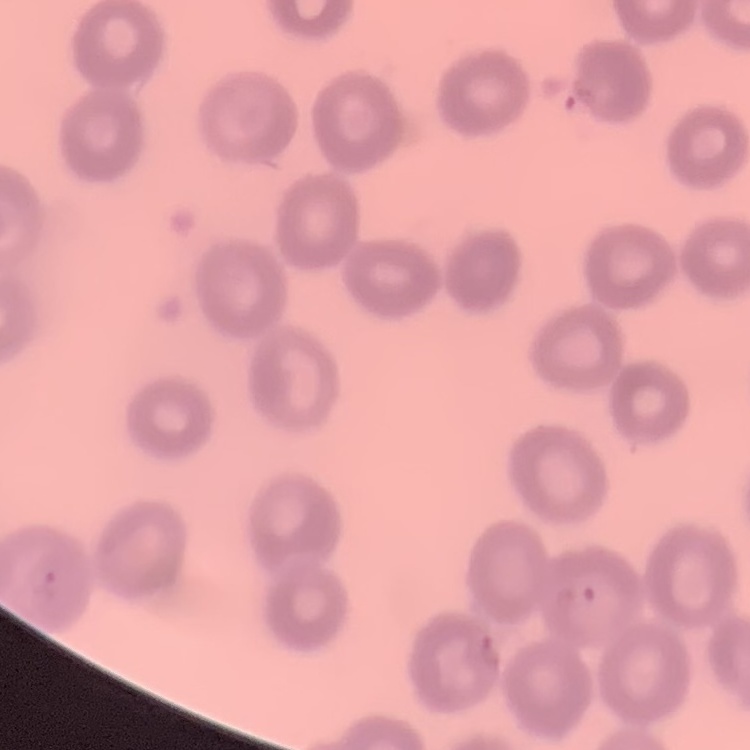
red blood cell morphology = no rouleaux formation
stain = Field's or Giemsa
preparation = thin blood smear
image type = one tile cut from a larger photomicrograph